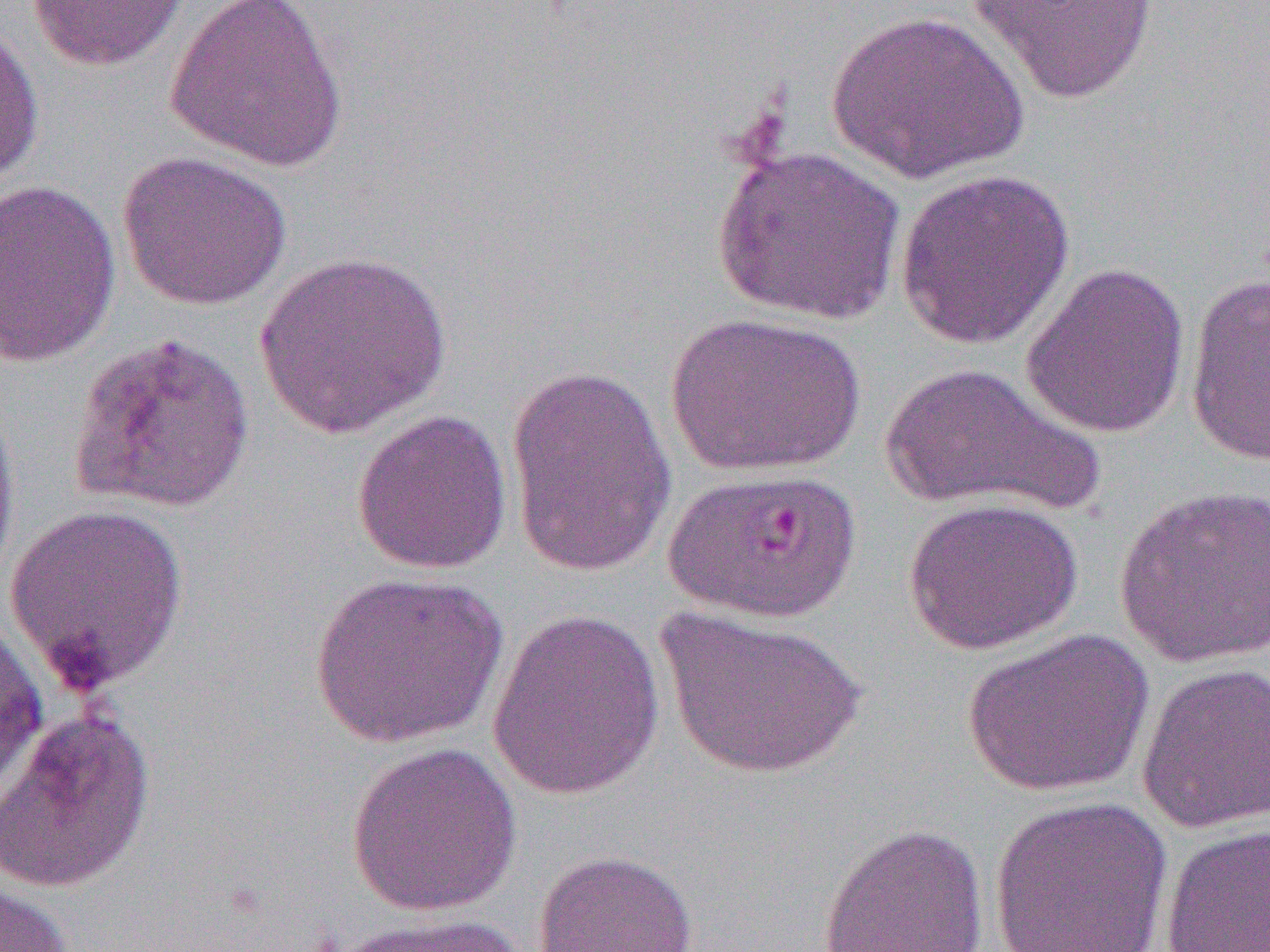

Approximate bounding boxes as (x1, y1, x2, y2) in pixels. Uninfected red blood cell locations: (25, 0, 191, 72), (165, 0, 351, 173), (966, 0, 1161, 105), (825, 10, 1030, 184), (0, 19, 45, 189), (711, 142, 906, 325), (116, 150, 292, 310), (894, 168, 1076, 350), (0, 179, 122, 368), (254, 249, 453, 439), (1021, 261, 1191, 440), (1185, 273, 1270, 466), (665, 312, 865, 477), (66, 331, 257, 516), (879, 362, 1103, 517), (505, 364, 677, 579), (0, 390, 22, 594), (351, 408, 514, 576), (1114, 484, 1270, 669), (903, 497, 1084, 654), (4, 501, 191, 693), (309, 571, 508, 748), (655, 606, 868, 780), (487, 607, 665, 801), (0, 620, 49, 806), (961, 627, 1154, 797), (1136, 662, 1270, 834), (0, 706, 156, 894), (346, 741, 523, 917), (987, 795, 1174, 952), (816, 822, 990, 952), (1159, 824, 1270, 951), (532, 849, 699, 952), (0, 880, 73, 952), (320, 912, 531, 952). Plasmodium falciparum-infected red blood cell locations: (663, 467, 865, 623). Slide-level diagnosis: Plasmodium falciparum. Captured at 1000x magnification. Image is 1270×952 pixels. Light microscopy. Single field of view. Thin blood smear.